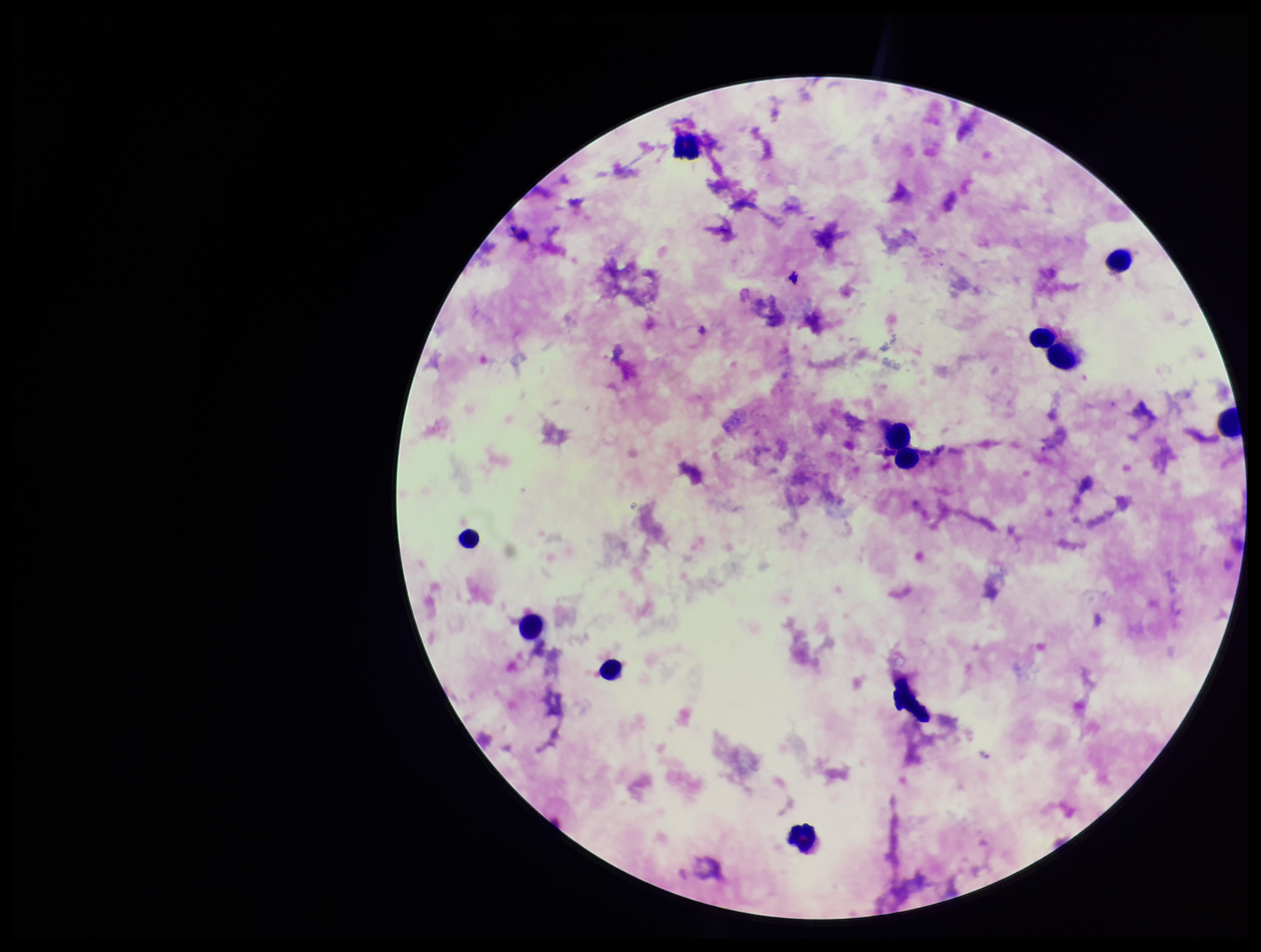
Summary:
  - Patient malaria status: positive
  - Leukocyte count: 10
  - Species reported for this patient: Plasmodium falciparum
  - Plasmodium parasites: none detected
  - Parasite count: 0
  - Image size: 1261×952 pixels
  - Preparation: thick smear
  - Stain: Giemsa
  - Capture: smartphone photograph through the microscope eyepiece
  - Field of view: one from this slide